Outline each blood parasite and name the species.
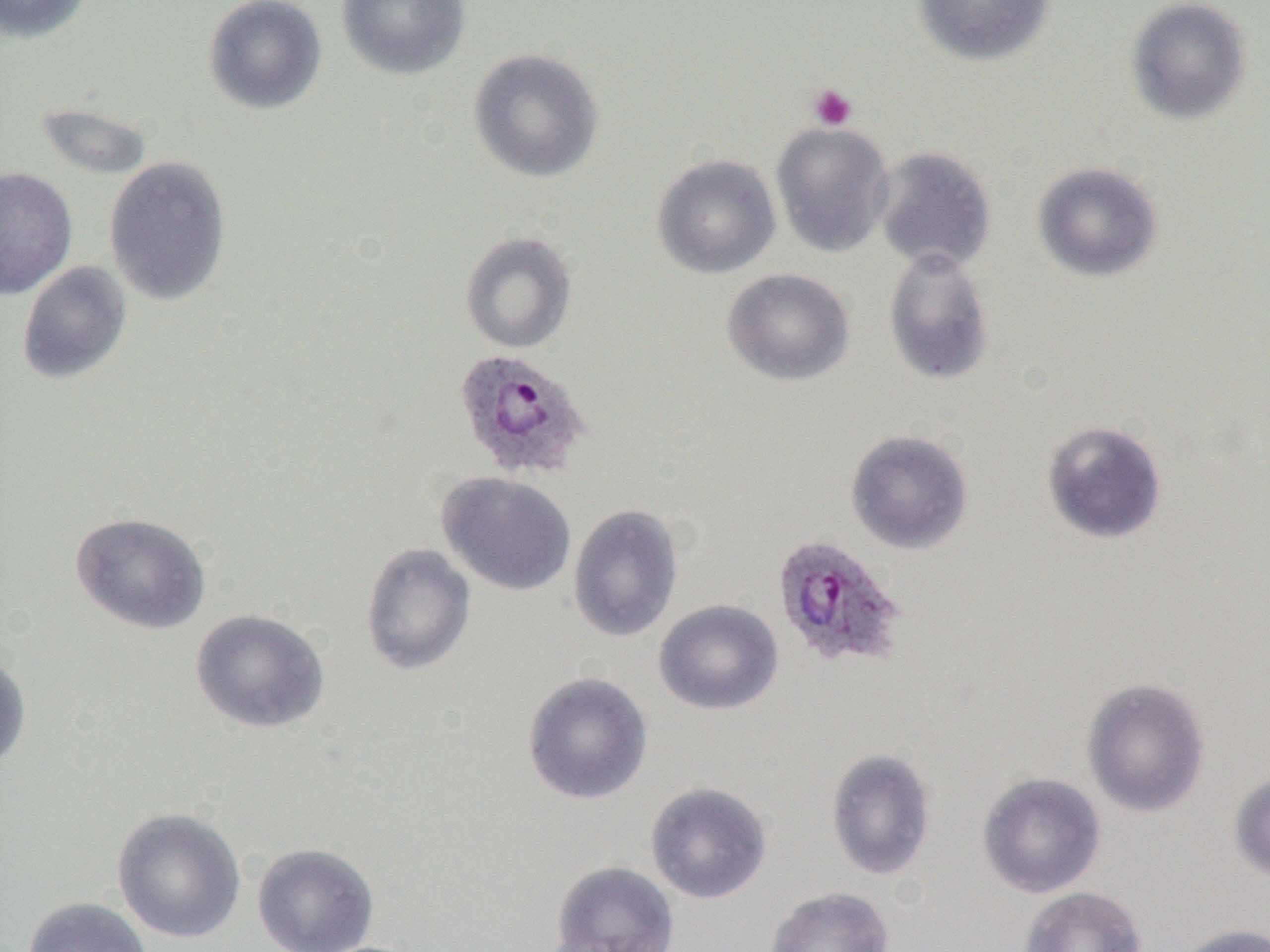

Approximate bounding boxes as (x1,y1)-(x2,y2) corner pairs in pixels.
Plasmodium ovale-infected red blood cells: (453,348)-(593,482), (772,534)-(907,671).
No Plasmodium falciparum, Plasmodium malariae, Plasmodium vivax, Babesia divergens, or Trypanosoma brucei observed.

slide-level diagnosis = Plasmodium ovale
field of view = single
preparation = thin blood film
platelet locations = approximate bounding boxes as (x1,y1)-(x2,y2) corner pairs in pixels: (808,84)-(858,131)
uninfected red blood cell locations = approximate bounding boxes as (x1,y1)-(x2,y2) corner pairs in pixels: (1,0)-(94,45), (202,0)-(328,115), (336,0)-(471,81), (913,0)-(1055,66), (1125,0)-(1252,125), (467,48)-(604,183), (33,102)-(155,182), (771,121)-(894,257), (873,145)-(996,272), (651,153)-(781,279), (103,156)-(232,306), (1032,161)-(1163,282), (0,166)-(78,300), (460,231)-(577,354), (883,247)-(996,387), (16,260)-(132,385), (722,268)-(855,386), (1041,419)-(1167,545), (845,429)-(974,555), (436,471)-(577,596), (567,503)-(684,643), (69,512)-(211,636), (359,542)-(476,676), (653,599)-(784,715), (190,608)-(330,733), (0,648)-(32,774), (521,671)-(654,805), (1081,676)-(1211,818), (826,747)-(938,881), (1229,771)-(1270,883), (977,772)-(1106,898), (645,782)-(772,904), (111,806)-(247,944), (252,842)-(380,952), (548,860)-(679,952), (764,886)-(895,952), (1017,886)-(1148,952), (22,896)-(154,952), (1173,922)-(1269,952)
modality = light microscopy
magnification = 1000x
image size = 1270×952 pixels